Outline each blood parasite and name the species.
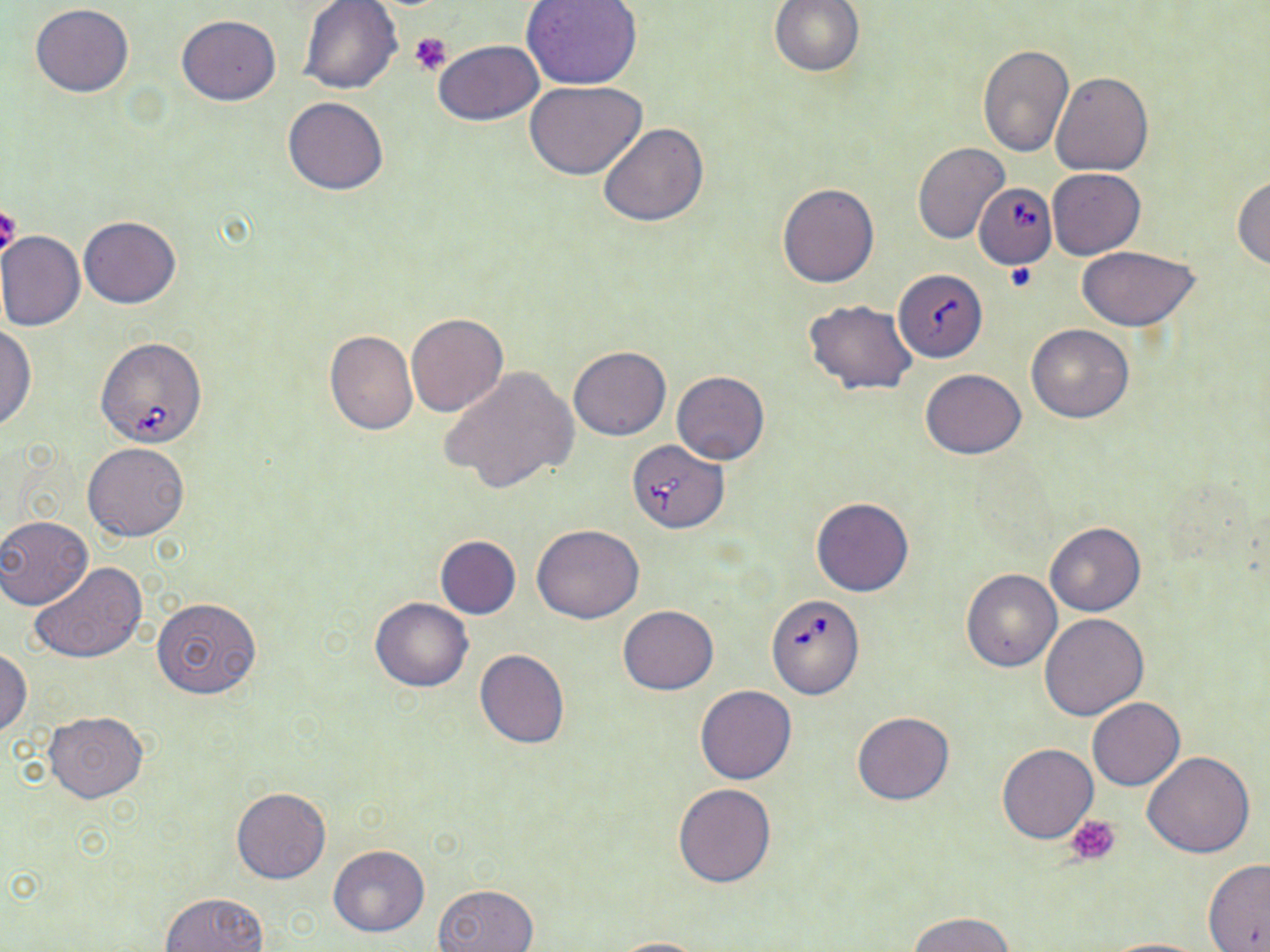
Approximate bounding boxes as [x1, y1, x2, y2] in pixels.
Babesia divergens-infected red blood cells: [974, 185, 1056, 269], [95, 336, 208, 448], [628, 440, 728, 533], [770, 597, 866, 700].
No Plasmodium falciparum, Plasmodium ovale, Plasmodium malariae, Plasmodium vivax, or Trypanosoma brucei observed.

slide-level diagnosis = Babesia divergens
modality = light microscopy
preparation = thin blood smear
field of view = single
uninfected red blood cell locations = approximate bounding boxes as [x1, y1, x2, y2] in pixels: [298, 0, 402, 96], [521, 0, 643, 88], [769, 0, 865, 76], [30, 4, 135, 98], [175, 15, 282, 105], [432, 40, 543, 125], [978, 45, 1073, 156], [1051, 71, 1153, 176], [526, 80, 647, 180], [283, 97, 390, 195], [598, 122, 709, 228], [913, 143, 1011, 245], [1047, 168, 1146, 259], [1232, 176, 1270, 271], [778, 182, 878, 287], [79, 216, 181, 308], [3, 229, 176, 324], [0, 231, 85, 331], [1075, 245, 1202, 330], [896, 270, 991, 362], [804, 299, 919, 394], [405, 312, 508, 417], [0, 324, 36, 432], [1026, 325, 1134, 423], [323, 329, 418, 436], [568, 346, 671, 440], [440, 365, 579, 494], [920, 369, 1025, 459], [672, 370, 770, 464], [82, 441, 189, 541], [811, 496, 914, 597], [0, 515, 92, 609], [1045, 523, 1145, 616], [532, 524, 644, 622], [435, 535, 521, 619], [30, 561, 148, 664], [960, 569, 1062, 672], [152, 596, 263, 699], [369, 597, 473, 692], [619, 605, 718, 693], [1040, 613, 1148, 720], [0, 648, 32, 737], [475, 649, 570, 747], [695, 685, 798, 784], [1087, 697, 1185, 790], [43, 712, 148, 803], [851, 712, 955, 805], [996, 743, 1099, 843], [1142, 750, 1256, 858], [673, 783, 777, 888], [231, 787, 331, 885], [327, 844, 430, 937], [1203, 858, 1270, 952], [433, 883, 539, 952], [160, 892, 269, 952], [909, 911, 1015, 952], [605, 937, 715, 951], [1096, 937, 1210, 951]
stain = May-Grünwald-Giemsa
magnification = 1000x
platelet locations = approximate bounding boxes as [x1, y1, x2, y2] in pixels: [410, 31, 453, 76], [0, 205, 22, 260], [1004, 262, 1039, 293], [1066, 814, 1121, 866]
image size = 1270×952 pixels